Locate every Plasmodium parasite.
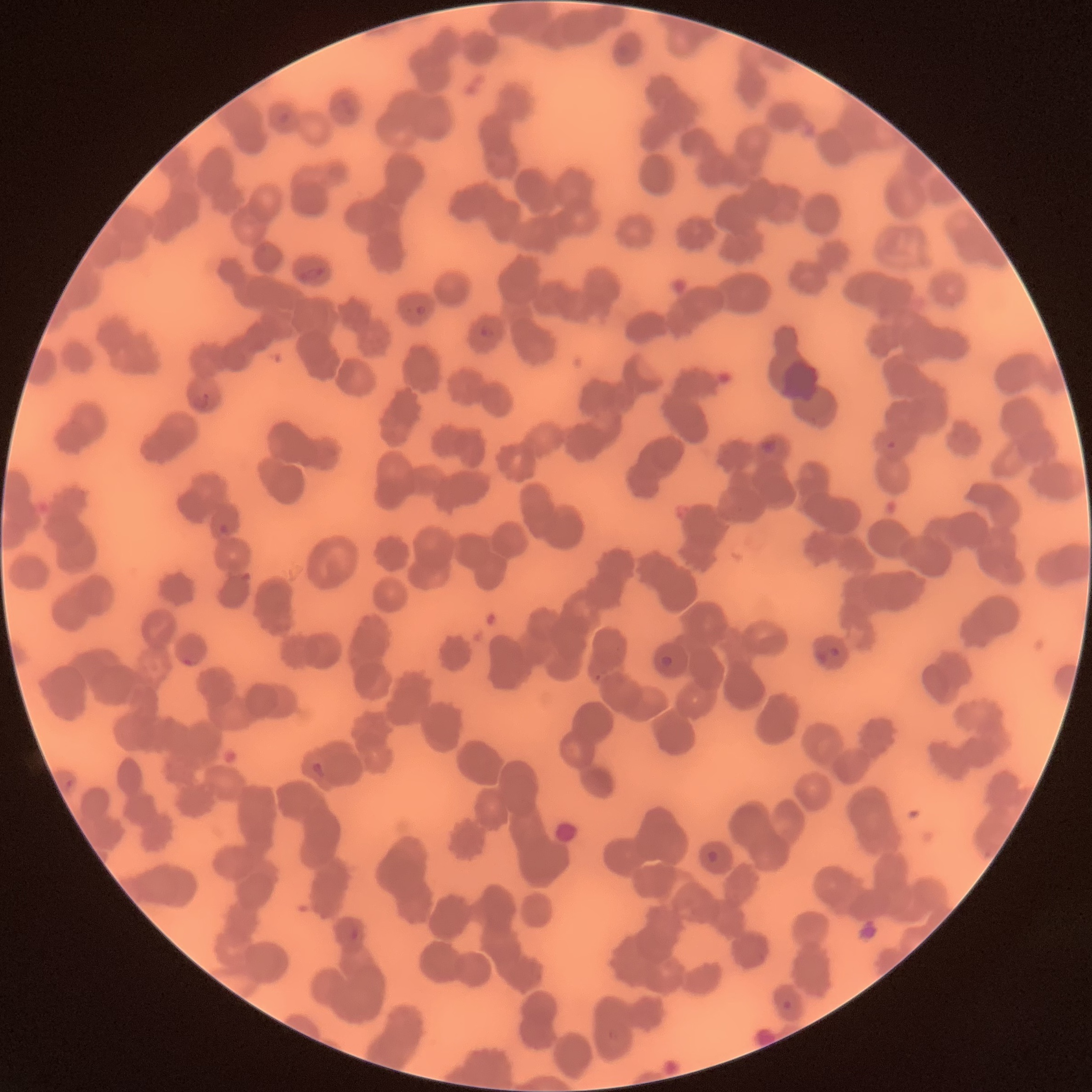
Approximate bounding boxes as named x1/y1/x2/y2 corners in pixels.
Plasmodium parasites: (x1=277, y1=111, x2=290, y2=125), (x1=298, y1=267, x2=325, y2=283), (x1=414, y1=304, x2=426, y2=315), (x1=480, y1=324, x2=495, y2=339), (x1=194, y1=391, x2=210, y2=409), (x1=762, y1=438, x2=777, y2=454), (x1=218, y1=522, x2=229, y2=534), (x1=815, y1=644, x2=841, y2=665), (x1=182, y1=652, x2=195, y2=667), (x1=659, y1=655, x2=674, y2=670), (x1=310, y1=761, x2=326, y2=779), (x1=64, y1=778, x2=74, y2=791), (x1=706, y1=849, x2=721, y2=864), (x1=349, y1=926, x2=360, y2=940), (x1=781, y1=999, x2=793, y2=1010).

The red blood cells show rouleaux formation. Thin blood smear. Light microscopy. Image is 1092×1092 pixels.